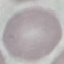

Malaria status: uninfected. Thin smear of blood. Giemsa stain. Acquired by smartphone through the microscope eyepiece. Cell patch, automatically extracted from a larger field of view and resized to 64 × 64 pixels.